Assess this cell for malaria.
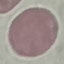

Uninfected.

Summary:
  - Image type: cell patch, automatically extracted from a larger field of view and resized to 64 × 64 pixels
  - Capture: smartphone camera at the microscope eyepiece
  - Stain: Giemsa
  - Preparation: thin blood smear